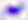
Summary:
  - Identification: Toxoplasma gondii
  - Magnification: 400x
  - Modality: micrograph